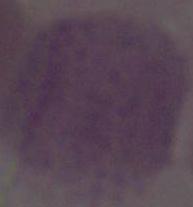
Summary:
  - Magnification: 1000x
  - Identification: red blood cell
  - Modality: photomicrograph